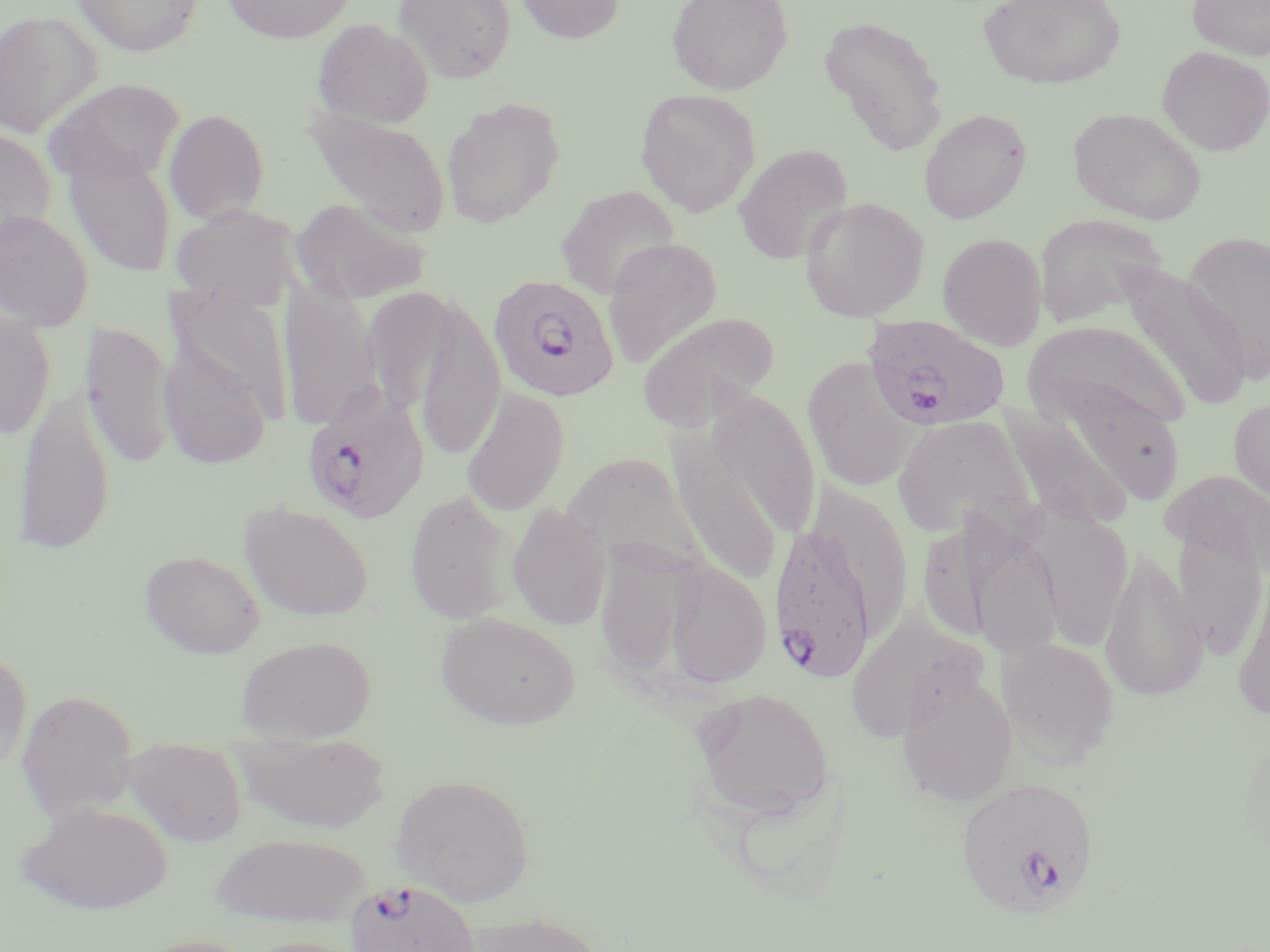

Approximate bounding boxes as (x1,y1)-(x2,y2) corner pairs in pixels. Plasmodium falciparum-infected red blood cell locations: (488,275)-(620,403), (863,315)-(1011,433), (301,381)-(429,525), (767,515)-(882,681), (955,777)-(1099,919), (344,879)-(480,952). Uninfected red blood cell locations: (71,0)-(205,57), (221,0)-(358,44), (393,0)-(517,84), (515,0)-(625,44), (667,0)-(793,95), (978,0)-(1125,90), (1187,0)-(1270,61), (0,10)-(101,139), (818,14)-(949,155), (311,18)-(434,129), (1157,46)-(1270,155), (45,79)-(186,186), (635,89)-(761,218), (440,97)-(566,229), (305,107)-(451,238), (1068,107)-(1208,225), (163,108)-(269,225), (918,108)-(1032,225), (0,126)-(56,249), (733,144)-(853,264), (64,147)-(175,279), (554,185)-(681,299), (799,196)-(930,322), (291,198)-(431,304), (170,204)-(302,310), (0,209)-(93,331), (1032,213)-(1168,330), (1183,229)-(1269,382), (937,233)-(1047,350), (602,237)-(723,369), (1118,264)-(1251,411), (278,281)-(380,431), (410,294)-(506,461), (0,302)-(54,440), (637,310)-(779,432), (82,321)-(177,471), (1023,321)-(1192,433), (158,325)-(273,472), (801,356)-(918,494), (14,379)-(116,556), (1057,383)-(1188,507), (461,387)-(570,517), (705,390)-(821,542), (1229,398)-(1270,512), (999,403)-(1134,530), (891,414)-(1034,538), (665,425)-(787,588), (562,451)-(700,568), (1162,468)-(1270,578), (404,489)-(522,626), (239,502)-(374,622), (507,502)-(613,632), (922,507)-(1068,666), (1038,512)-(1131,654), (1172,522)-(1267,661), (594,543)-(696,681), (1100,545)-(1208,703), (140,550)-(266,659), (663,559)-(772,688), (1232,568)-(1270,720), (845,611)-(983,742), (435,612)-(581,729), (235,635)-(376,744), (996,637)-(1119,767), (0,647)-(32,777), (897,673)-(1018,806), (688,685)-(835,825), (16,690)-(139,820), (1237,725)-(1270,875), (235,731)-(391,833), (123,738)-(249,847), (391,773)-(534,907), (17,800)-(174,915), (209,833)-(372,927), (452,911)-(611,952), (131,934)-(258,952), (236,935)-(366,952). Slide-level diagnosis: Plasmodium falciparum. Image is 1270×952 pixels. Thin blood smear. Optical microscopy. Captured at 1000x magnification. Single field of view. May-Grünwald-Giemsa-stained preparation.